State which parasite is depicted.
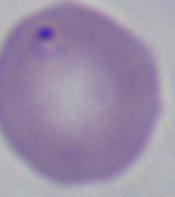
This is Babesia.

magnification = 1000x
modality = photomicrograph